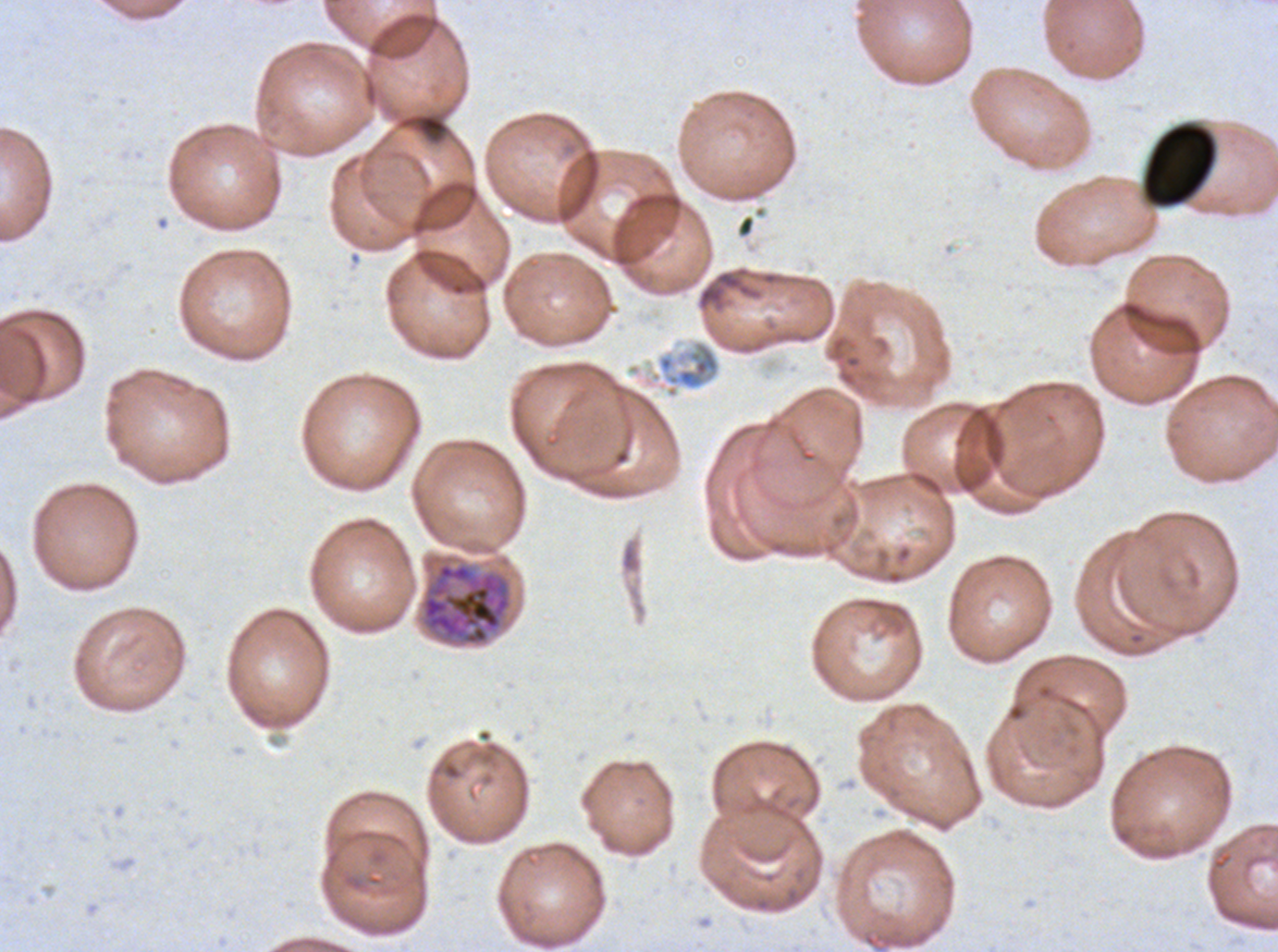

Approximate bounding rectangles given as corner coordinates in pixels from the top-left.
Summary:
  - Early schizont locations: (x1=420, y1=561, x2=513, y2=647)
  - Debris locations: (x1=1142, y1=122, x2=1217, y2=208), (x1=625, y1=337, x2=722, y2=400)
  - Image size: 1278×952 pixels
  - Preparation: thin blood film
  - Specimen: P. falciparum cultured ex vivo for 24 to 48 hours, from a patient in The Gambia
  - Stain: Giemsa
  - Field of view: one sub-image of a larger composite